Mark where platelets are.
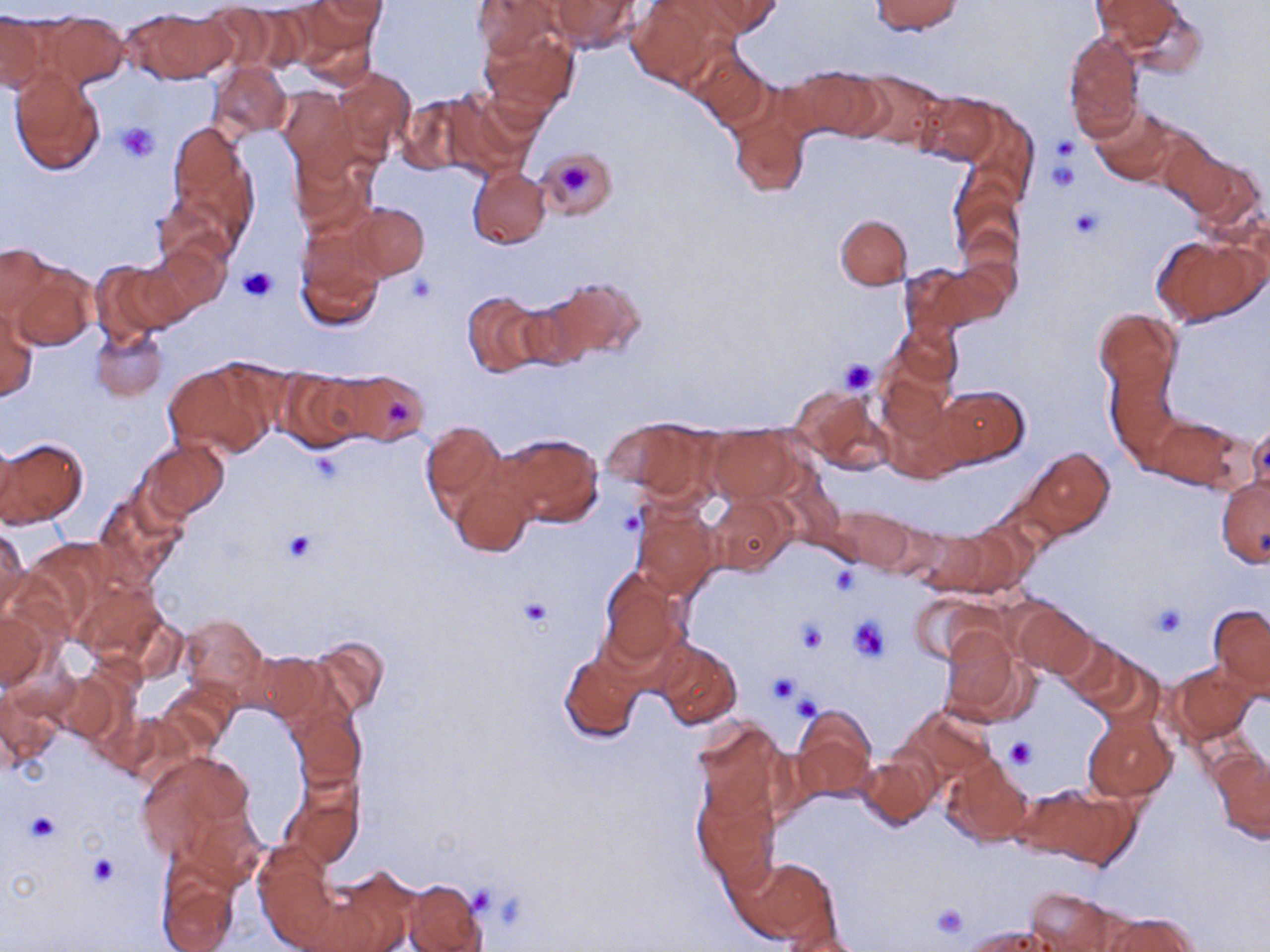

Approximate bounding boxes as (x1,y1)-(x2,y2) corner pairs in pixels.
Platelets: (116,123)-(161,162), (1051,134)-(1078,162), (1047,160)-(1082,193), (558,161)-(588,194), (1069,208)-(1103,240), (239,264)-(276,303), (408,271)-(438,303), (839,359)-(877,395), (386,397)-(414,427), (281,527)-(319,564), (829,566)-(860,595), (519,598)-(553,630), (1151,602)-(1188,638), (848,617)-(891,662), (796,620)-(829,653), (767,672)-(799,703), (791,692)-(822,722), (1005,737)-(1036,769), (26,812)-(61,843), (90,854)-(119,885), (468,886)-(497,918), (929,901)-(970,942).

slide-level diagnosis = negative for blood parasites
stain = May-Grünwald-Giemsa
magnification = 1000x
modality = optical microscopy
preparation = thin blood film
uninfected red blood cell locations = approximate bounding boxes as (x1,y1)-(x2,y2) corner pairs in pixels: (548,0)-(640,52), (626,0)-(724,90), (871,0)-(963,35), (1092,0)-(1184,50), (293,1)-(385,66), (315,1)-(388,24), (471,1)-(562,61), (698,1)-(780,37), (1117,5)-(1207,75), (125,8)-(232,83), (44,12)-(128,89), (0,14)-(45,93), (479,24)-(579,120), (1063,33)-(1143,141), (686,49)-(774,131), (209,62)-(291,138), (792,66)-(885,143), (334,67)-(415,157), (9,68)-(106,176), (855,70)-(948,150), (279,87)-(356,173), (441,88)-(539,178), (919,93)-(999,165), (397,94)-(480,176), (1091,104)-(1177,184), (728,107)-(811,198), (163,120)-(257,241), (289,145)-(377,238), (1167,146)-(1260,230), (528,147)-(617,227), (468,166)-(551,248), (948,175)-(1022,266), (343,202)-(429,282), (836,213)-(912,290), (1151,235)-(1264,325), (294,239)-(383,335), (142,241)-(228,319), (0,242)-(58,321), (94,260)-(185,341), (11,262)-(96,350), (900,264)-(980,343), (551,275)-(644,365), (512,289)-(600,371), (463,290)-(547,378), (1,301)-(39,404), (1096,309)-(1180,400), (891,321)-(962,389), (91,325)-(167,402), (162,361)-(273,457), (277,369)-(372,453), (333,369)-(431,447), (1108,370)-(1178,462), (874,375)-(959,475), (932,384)-(1029,469), (794,386)-(888,471), (1148,415)-(1242,491), (606,417)-(717,502), (420,419)-(509,522), (1245,424)-(1270,500), (708,426)-(802,502), (493,430)-(604,530), (0,437)-(18,526), (1,437)-(87,527), (139,438)-(230,521), (1024,446)-(1114,538), (449,466)-(537,559), (1217,475)-(1269,566), (93,488)-(188,585), (706,491)-(795,577), (630,500)-(721,600), (833,507)-(914,571), (0,524)-(28,618), (918,528)-(1020,596), (599,567)-(686,674), (71,576)-(168,667), (910,592)-(999,666), (1012,600)-(1095,680), (1208,604)-(1269,693), (1,609)-(48,691), (179,612)-(267,702), (938,623)-(1035,726), (1052,632)-(1133,707), (305,635)-(391,719), (655,639)-(742,730), (1076,646)-(1165,729), (559,648)-(644,744), (245,651)-(327,724), (1167,662)-(1257,743), (50,668)-(133,748), (1,677)-(70,768), (156,682)-(239,756), (286,692)-(367,790), (897,705)-(997,789), (792,706)-(879,804), (117,713)-(201,789), (1083,714)-(1177,803), (692,720)-(789,825), (1213,750)-(1270,841), (138,752)-(256,870), (855,754)-(938,830), (942,756)-(1033,845), (282,773)-(365,871), (693,785)-(779,888), (1012,787)-(1113,862), (254,847)-(341,949), (154,855)-(238,952), (732,856)-(836,945), (320,867)-(420,950), (403,878)-(487,952), (1025,888)-(1128,951), (1099,911)-(1199,952), (963,924)-(1054,950)
image size = 1270×952 pixels
field of view = one of a larger specimen